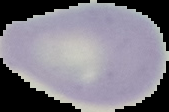
Summary:
  - Malaria status: uninfected
  - Preparation: thin blood smear
  - Image size: 169×112 pixels
  - Image type: segmented cell region with the area outside set to black